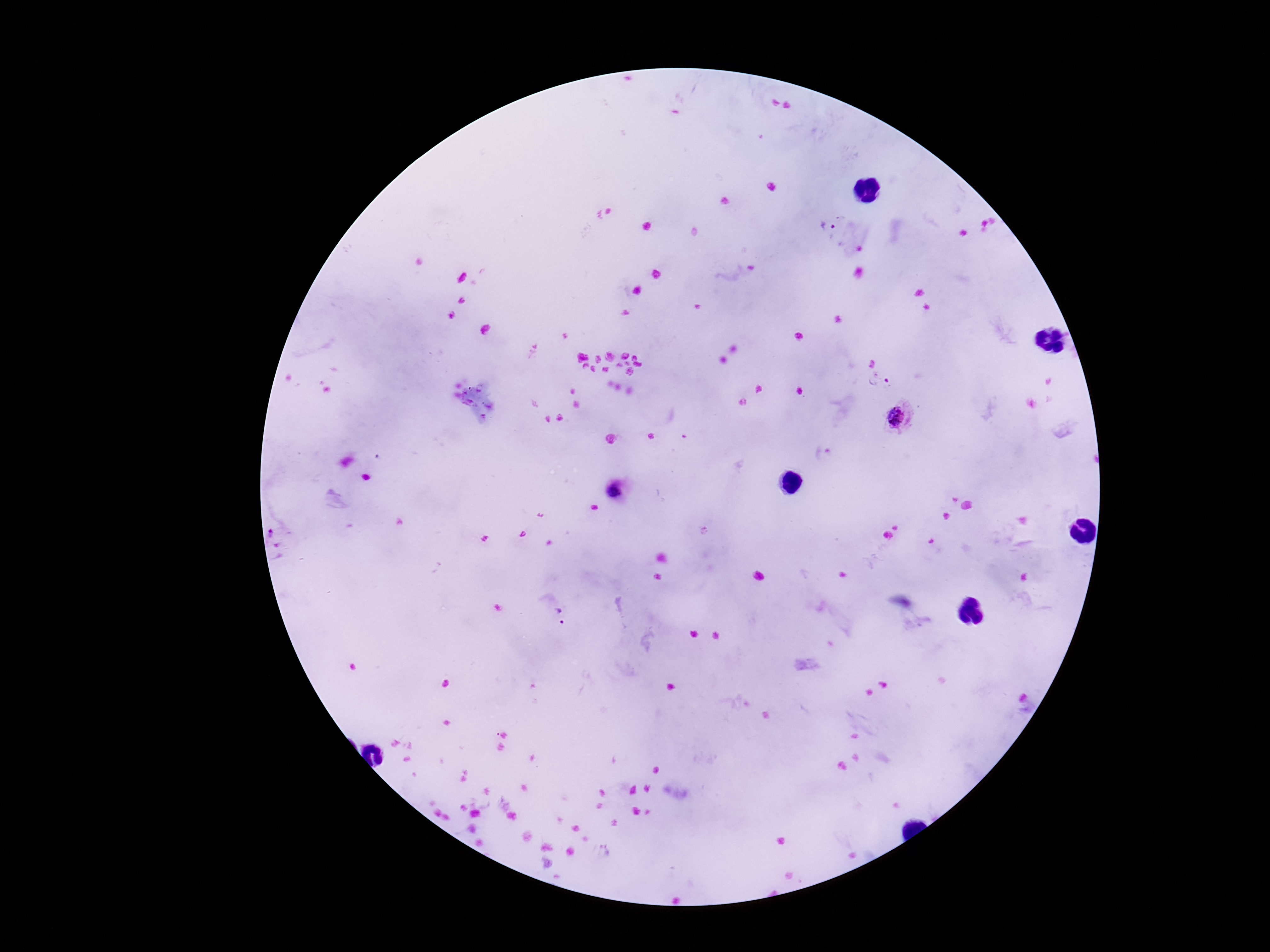

Approximate centers as {x, y} in pixels.
Summary:
  - Plasmodium parasite locations: {830, 228}, {879, 382}, {899, 417}, {823, 453}, {614, 493}, {560, 617}
  - Field of view: single
  - Capture: smartphone camera through the microscope eyepiece
  - Preparation: thick blood smear
  - Stain: Giemsa
  - Magnification: 100x
  - Image size: 1270×952 pixels
  - Patient malaria status: infected